Assess the morphology of the red blood cells.
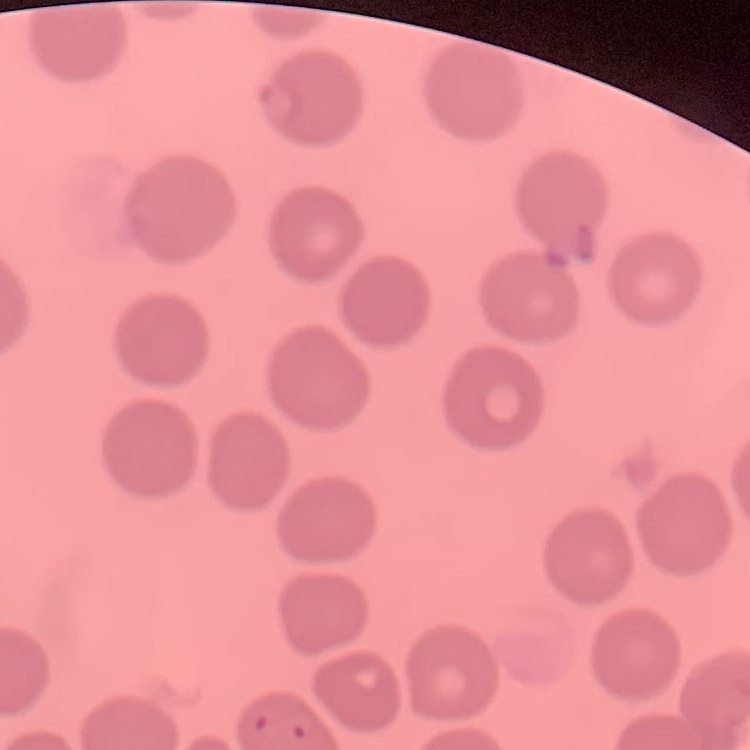
No rouleaux formation.

Thin blood film. Field's or Giemsa stain. One tile cut from a larger photomicrograph.